State which parasite is depicted.
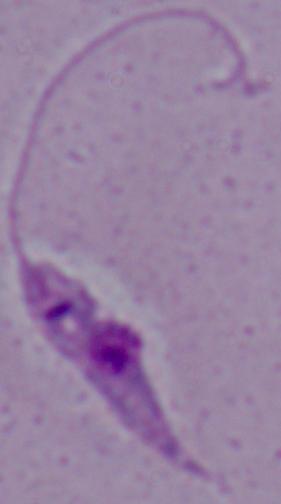

This is Leishmania.

Summary:
  - Magnification: 1000x
  - Modality: micrograph